Report the malaria status of this cell.
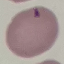

It is uninfected.

image_type: automatically extracted cell patch, resized to 64 × 64 pixels
capture: smartphone camera at the microscope eyepiece
stain: Giemsa
preparation: thin smear